Report the malaria status of this cell.
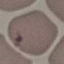
It is uninfected.

{
  "image_type": "automatically extracted cell patch, resized to 64 × 64 pixels",
  "capture": "smartphone through the microscope eyepiece",
  "preparation": "thin blood smear",
  "stain": "Giemsa"
}